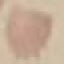

malaria status = uninfected
preparation = thin blood film
capture = smartphone through the microscope eyepiece
stain = Giemsa
image type = cell patch, automatically extracted from a larger field of view and resized to 64 × 64 pixels